Name the parasite shown.
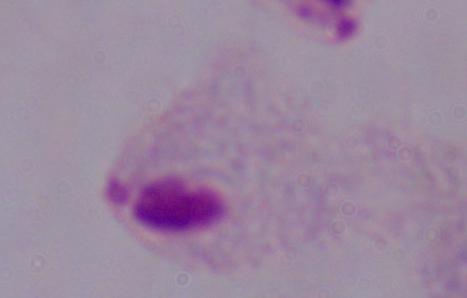
A trichomonad.

magnification = 1000x
modality = photomicrograph